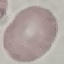

Summary:
  - Result: no malaria parasites seen
  - Stain: Giemsa
  - Capture: smartphone camera at the microscope eyepiece
  - Preparation: thin blood smear
  - Image type: automatically extracted cell patch, resized to 64 × 64 pixels